State the blood parasite species.
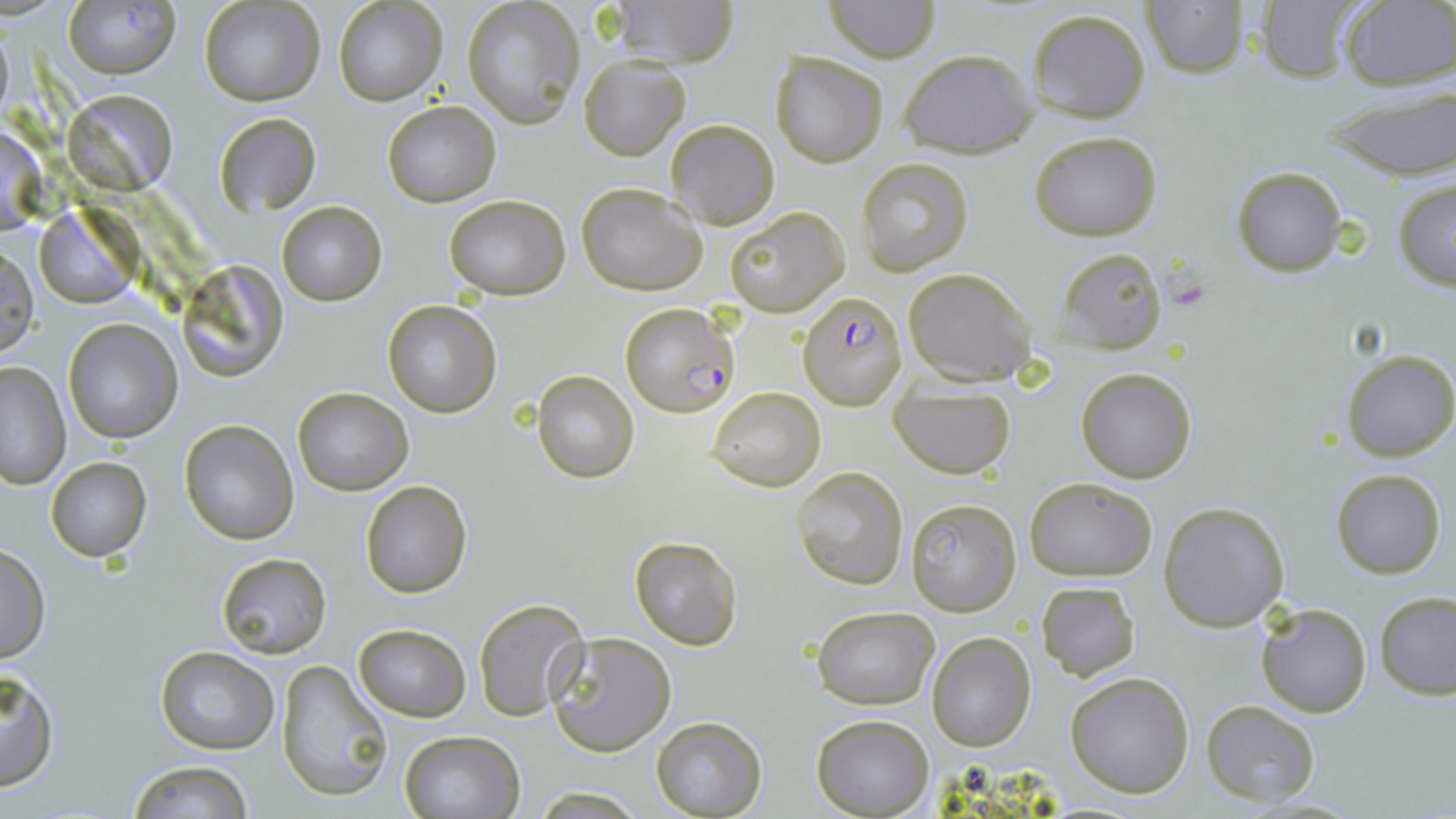
Plasmodium falciparum.

Approximate bounding boxes as (x1,y1)-(x2,y2) corner pairs in pixels. Uninfected red blood cell locations: (606,0)-(741,67), (823,0)-(941,64), (200,1)-(323,106), (333,1)-(446,107), (1253,1)-(1368,85), (63,2)-(178,79), (462,2)-(583,128), (1142,2)-(1248,78), (1337,2)-(1456,90), (1027,8)-(1150,122), (897,49)-(1040,157), (769,51)-(889,167), (578,54)-(690,160), (1323,83)-(1456,181), (64,88)-(175,190), (382,101)-(500,206), (212,112)-(320,218), (666,119)-(779,229), (0,123)-(45,234), (1029,131)-(1162,240), (857,156)-(973,275), (1231,167)-(1346,276), (1392,180)-(1456,290), (576,183)-(708,295), (443,195)-(569,300), (277,201)-(385,305), (724,207)-(849,316), (35,208)-(137,309), (1,247)-(37,358), (1055,247)-(1168,352), (175,258)-(289,381), (903,267)-(1036,385), (382,302)-(501,418), (62,319)-(181,442), (1341,350)-(1456,461), (0,363)-(71,488), (1074,366)-(1197,482), (532,371)-(638,483), (889,385)-(1017,478), (293,387)-(412,495), (707,387)-(824,492), (180,420)-(298,545), (44,458)-(152,561), (792,466)-(908,589), (1331,468)-(1447,580), (1025,475)-(1158,581), (361,481)-(472,598), (906,497)-(1021,616), (1159,501)-(1291,632), (629,536)-(744,651), (0,544)-(50,664), (215,552)-(333,659), (1037,581)-(1140,681), (1375,590)-(1456,699), (474,599)-(590,721), (1256,603)-(1372,717), (811,607)-(937,710), (353,624)-(470,720), (545,631)-(677,756), (926,632)-(1036,753), (154,645)-(277,754), (277,659)-(395,803), (0,667)-(59,791), (1065,672)-(1194,798), (1201,701)-(1319,805), (811,715)-(933,817), (651,717)-(767,816), (398,730)-(524,818), (125,760)-(256,818), (529,788)-(645,818). Plasmodium falciparum-infected red blood cell locations: (798,292)-(906,410), (620,302)-(738,418). May-Grünwald-Giemsa stain. 1000x magnification. Single field of view. Image is 1456×819 pixels. Light microscopy. Thin blood film.